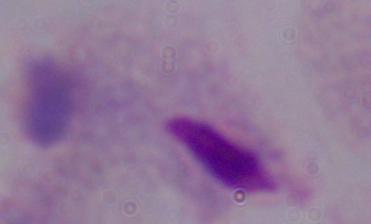

Summary:
  - Magnification: 1000x
  - Identification: trichomonad
  - Modality: micrograph